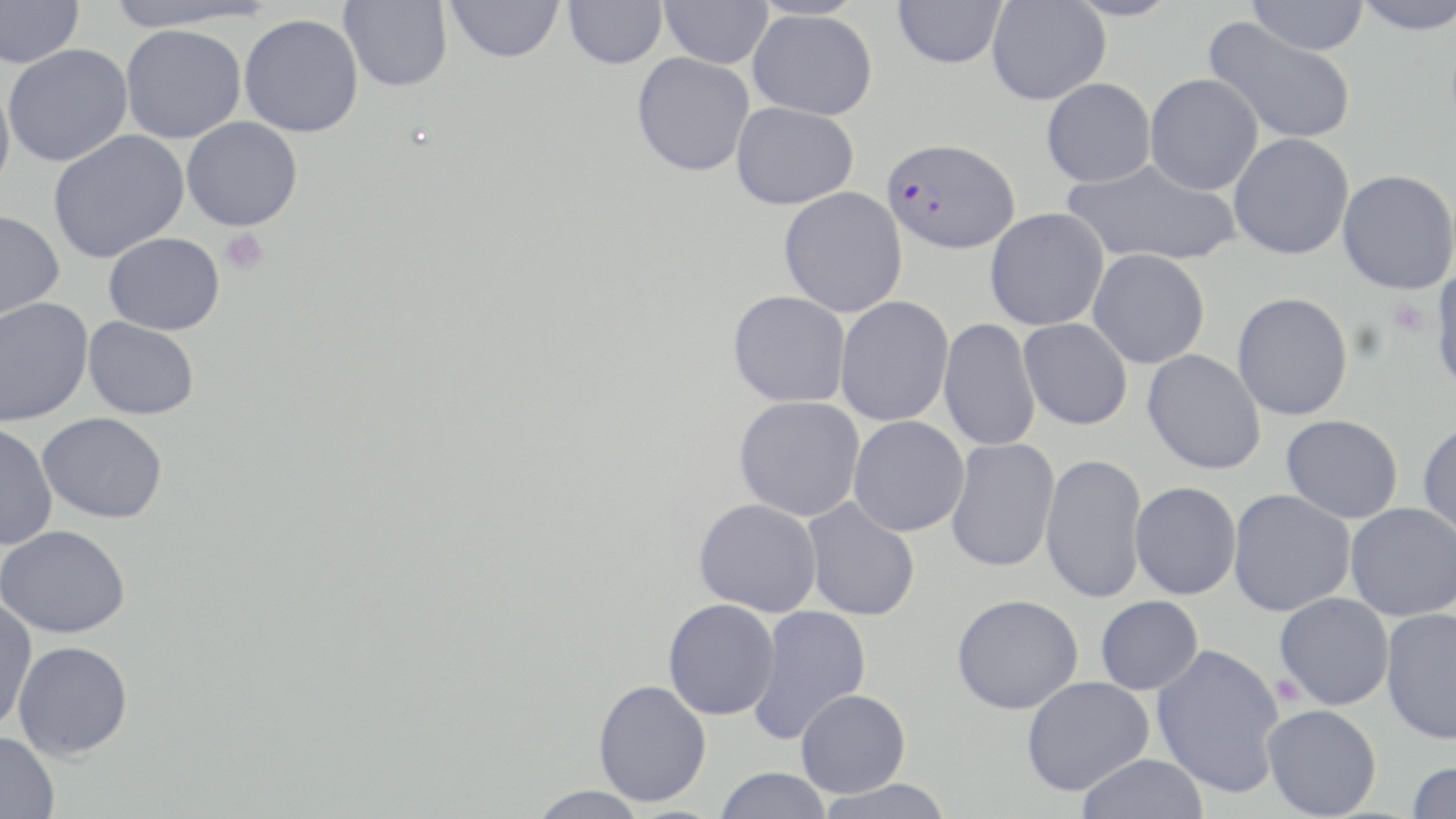

slide_level_diagnosis: Plasmodium falciparum
stain: May-Grünwald-Giemsa
plasmodium_falciparum_infected_red_blood_cell_locations: 'approximate bounding boxes as named x1/y1/x2/y2 corners in pixels: (x1=882, y1=137, x2=1019, y2=254)'
platelet_locations: 'approximate bounding boxes as named x1/y1/x2/y2 corners in pixels: (x1=220, y1=228, x2=270, y2=276), (x1=1388, y1=297, x2=1432, y2=338), (x1=1270, y1=675, x2=1305, y2=706)'
magnification: 1000x
uninfected_red_blood_cell_locations: 'approximate bounding boxes as named x1/y1/x2/y2 corners in pixels: (x1=0, y1=0, x2=85, y2=68), (x1=100, y1=0, x2=271, y2=32), (x1=339, y1=0, x2=452, y2=92), (x1=447, y1=0, x2=564, y2=63), (x1=564, y1=0, x2=667, y2=69), (x1=659, y1=0, x2=773, y2=69), (x1=892, y1=0, x2=1007, y2=69), (x1=987, y1=0, x2=1110, y2=105), (x1=1245, y1=0, x2=1370, y2=55), (x1=1348, y1=0, x2=1456, y2=35), (x1=748, y1=9, x2=878, y2=120), (x1=239, y1=14, x2=363, y2=136), (x1=1203, y1=17, x2=1356, y2=145), (x1=121, y1=24, x2=246, y2=143), (x1=2, y1=44, x2=132, y2=167), (x1=632, y1=52, x2=755, y2=176), (x1=1144, y1=73, x2=1263, y2=195), (x1=0, y1=76, x2=16, y2=196), (x1=1041, y1=78, x2=1156, y2=187), (x1=731, y1=102, x2=859, y2=210), (x1=181, y1=117, x2=303, y2=231), (x1=47, y1=130, x2=190, y2=262), (x1=1228, y1=132, x2=1354, y2=260), (x1=1063, y1=158, x2=1241, y2=267), (x1=1337, y1=169, x2=1455, y2=294), (x1=778, y1=186, x2=908, y2=317), (x1=985, y1=207, x2=1110, y2=331), (x1=0, y1=210, x2=65, y2=324), (x1=104, y1=232, x2=225, y2=335), (x1=1087, y1=249, x2=1210, y2=368), (x1=1429, y1=264, x2=1456, y2=398), (x1=728, y1=290, x2=851, y2=408), (x1=1232, y1=292, x2=1354, y2=421), (x1=835, y1=296, x2=954, y2=426), (x1=0, y1=297, x2=94, y2=427), (x1=83, y1=316, x2=199, y2=419), (x1=938, y1=318, x2=1041, y2=452), (x1=1018, y1=318, x2=1133, y2=430), (x1=1141, y1=349, x2=1267, y2=476), (x1=734, y1=396, x2=865, y2=521), (x1=38, y1=412, x2=168, y2=523), (x1=1281, y1=414, x2=1404, y2=523), (x1=849, y1=415, x2=970, y2=536), (x1=1417, y1=419, x2=1456, y2=541), (x1=0, y1=423, x2=58, y2=550), (x1=945, y1=438, x2=1059, y2=572), (x1=1040, y1=453, x2=1149, y2=604), (x1=1130, y1=481, x2=1242, y2=599), (x1=1228, y1=489, x2=1356, y2=616), (x1=801, y1=497, x2=920, y2=621), (x1=693, y1=498, x2=822, y2=616), (x1=1345, y1=503, x2=1456, y2=621), (x1=1, y1=525, x2=130, y2=638), (x1=1274, y1=592, x2=1394, y2=710), (x1=952, y1=593, x2=1084, y2=714), (x1=1095, y1=595, x2=1204, y2=695), (x1=0, y1=598, x2=38, y2=732), (x1=663, y1=598, x2=780, y2=720), (x1=746, y1=606, x2=871, y2=745), (x1=1381, y1=607, x2=1456, y2=744), (x1=13, y1=640, x2=133, y2=759), (x1=1151, y1=643, x2=1286, y2=798), (x1=1021, y1=677, x2=1154, y2=796), (x1=593, y1=679, x2=712, y2=807), (x1=796, y1=688, x2=910, y2=797), (x1=1262, y1=704, x2=1382, y2=818), (x1=0, y1=731, x2=60, y2=819), (x1=1077, y1=753, x2=1209, y2=819), (x1=1406, y1=760, x2=1456, y2=819), (x1=714, y1=767, x2=833, y2=819), (x1=814, y1=778, x2=956, y2=819), (x1=525, y1=786, x2=650, y2=818)'
preparation: thin blood film
image_size: 1456×819 pixels
modality: light microscopy
field_of_view: single